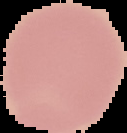

Summary:
  - Image type: cell region segmented out of the field of view; surrounding area masked to black
  - Preparation: thin blood film
  - Malaria status: uninfected
  - Image size: 127×133 pixels